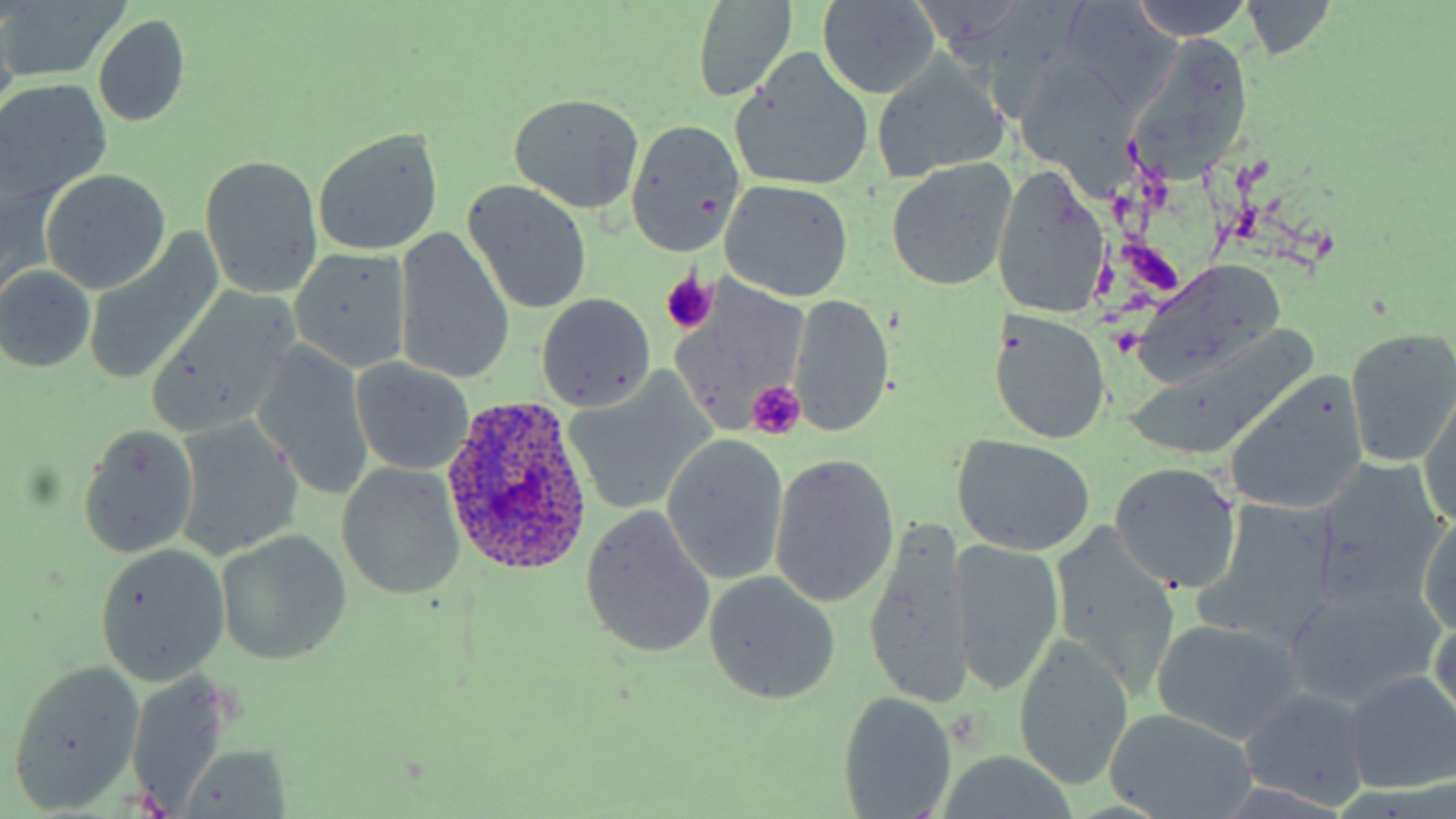
Summary:
  - Coordinate format: approximate bounding boxes as [x1, y1, x2, y2] in pixels
  - Uninfected red blood cell locations: [1125, 0, 1255, 41], [0, 1, 132, 81], [689, 1, 800, 103], [1237, 1, 1340, 61], [816, 2, 943, 99], [1057, 3, 1181, 113], [94, 15, 191, 128], [1129, 38, 1254, 179], [732, 57, 874, 191], [872, 57, 1011, 183], [1013, 63, 1138, 183], [1, 78, 111, 202], [507, 92, 646, 215], [625, 119, 744, 258], [311, 125, 444, 258], [200, 155, 323, 298], [885, 161, 1016, 289], [993, 164, 1109, 320], [40, 169, 172, 293], [463, 180, 592, 316], [722, 180, 854, 304], [393, 226, 514, 387], [289, 247, 412, 375], [83, 249, 215, 384], [1132, 261, 1286, 386], [1, 263, 98, 374], [666, 281, 810, 437], [535, 293, 657, 412], [789, 293, 894, 440], [146, 296, 300, 435], [989, 311, 1111, 446], [1345, 326, 1456, 468], [250, 340, 375, 503], [347, 358, 476, 476], [1227, 375, 1371, 516], [565, 378, 713, 516], [1418, 390, 1456, 529], [174, 416, 304, 561], [77, 422, 199, 557], [661, 433, 790, 586], [952, 435, 1095, 557], [769, 451, 901, 610], [1314, 457, 1450, 607], [336, 461, 465, 601], [1108, 462, 1242, 594], [580, 505, 717, 661], [1205, 510, 1337, 645], [1417, 513, 1456, 633], [1051, 522, 1181, 695], [865, 523, 970, 709], [217, 530, 351, 665], [951, 538, 1064, 698], [93, 543, 231, 685], [703, 571, 840, 703], [1280, 586, 1441, 709], [1429, 610, 1455, 731], [1152, 618, 1305, 744], [1014, 637, 1132, 793], [8, 663, 143, 808], [1342, 670, 1456, 794], [125, 671, 234, 809], [1237, 686, 1371, 810], [838, 691, 957, 819], [1103, 711, 1257, 818], [180, 746, 292, 818]
  - Platelet locations: [657, 270, 716, 333], [744, 380, 804, 439]
  - Plasmodium ovale-infected red blood cell locations: [440, 396, 595, 576]
  - Slide-level diagnosis: Plasmodium ovale
  - Image size: 1456×819 pixels
  - Stain: May-Grünwald-Giemsa
  - Magnification: 1000x
  - Preparation: thin blood film
  - Modality: light microscopy
  - Field of view: one of a larger specimen